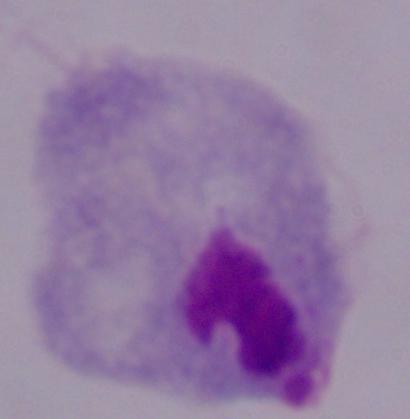 Micrograph. 1000x magnification. A trichomonad is shown.